Describe the morphology of the erythrocytes.
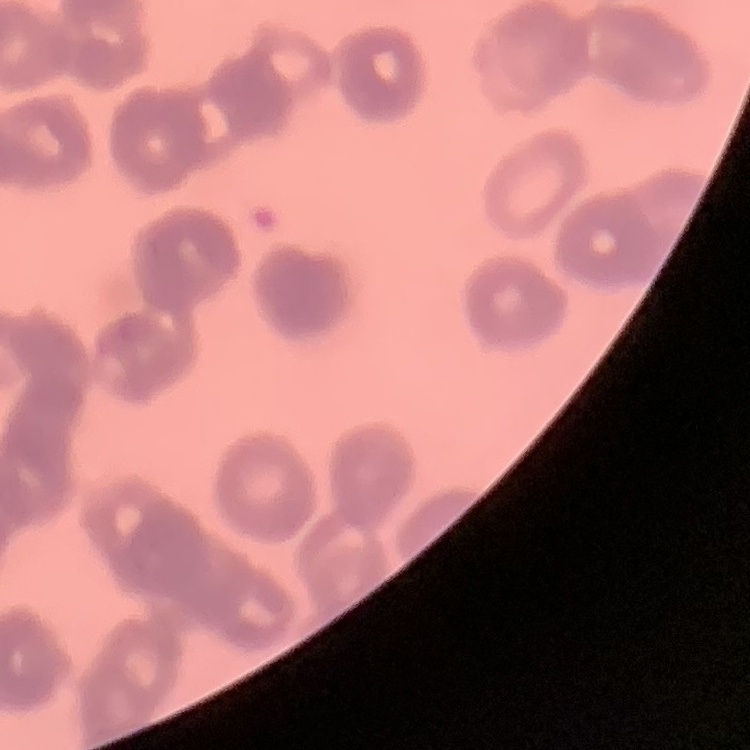
They show rouleaux formation.

Thin blood film. Stained with either Field's or Giemsa. One tile cut from a larger photomicrograph.